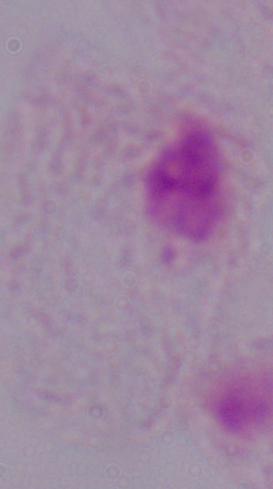
Summary:
  - Modality: photomicrograph
  - Identification: trichomonad
  - Magnification: 1000x